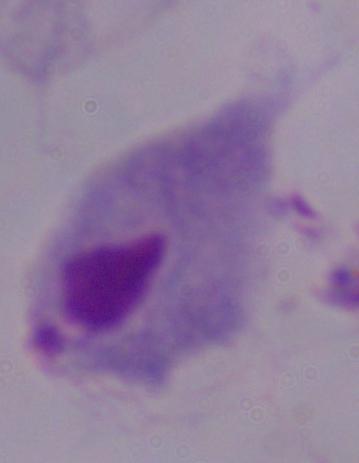
modality = photomicrograph
identification = trichomonad
magnification = 1000x